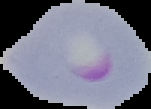

Summary:
  - Result: malaria parasites detected
  - Image type: segmented cell region on a black background
  - Image size: 151×109 pixels
  - Preparation: thin blood film